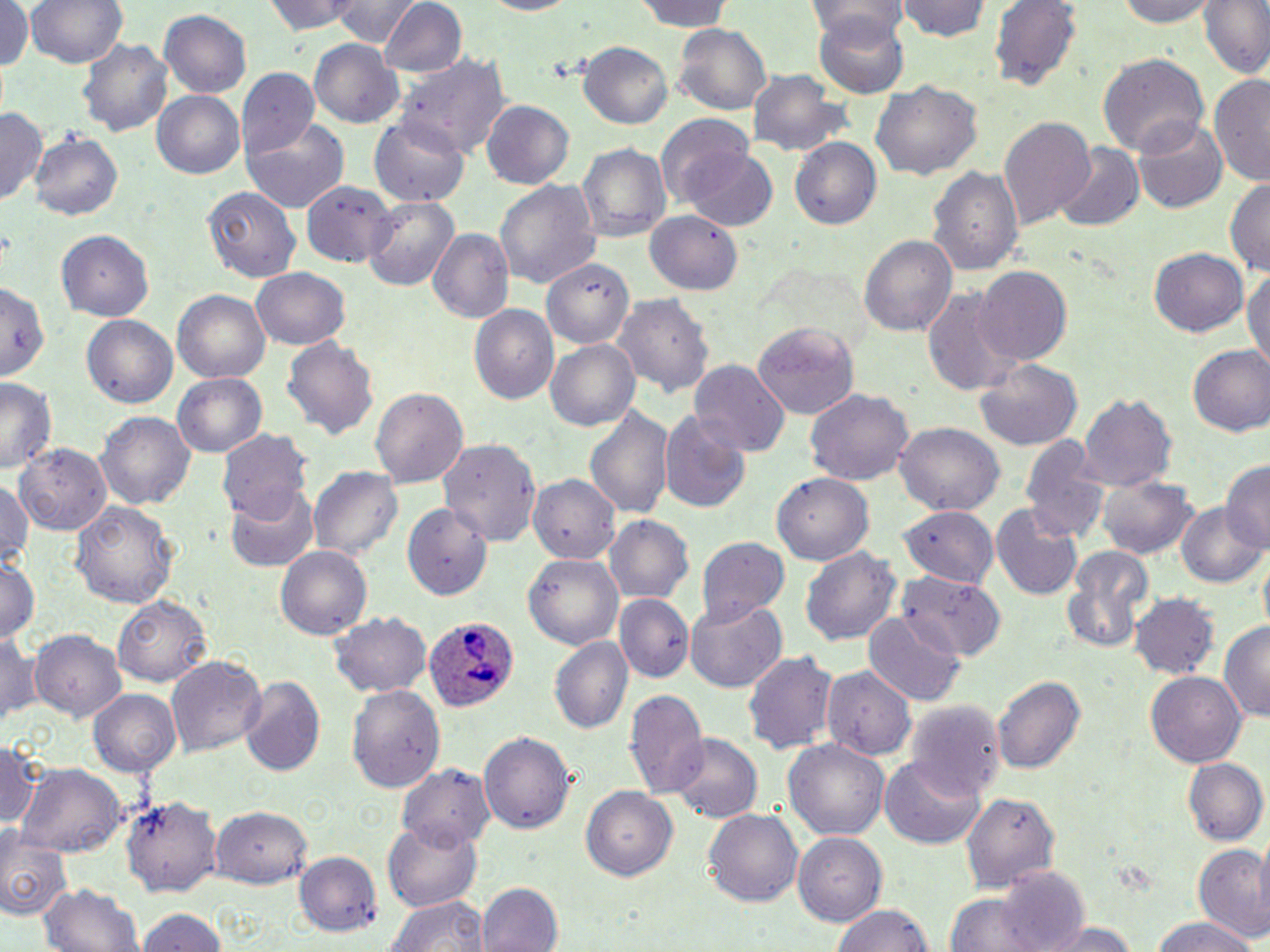
Summary:
  - Coordinate format: approximate bounding boxes as named x1/y1/x2/y2 corners in pixels
  - Uninfected red blood cell locations: (x1=28, y1=0, x2=127, y2=70), (x1=264, y1=0, x2=363, y2=35), (x1=330, y1=0, x2=416, y2=47), (x1=472, y1=0, x2=583, y2=17), (x1=626, y1=0, x2=736, y2=31), (x1=1111, y1=0, x2=1221, y2=26), (x1=1197, y1=0, x2=1270, y2=82), (x1=0, y1=1, x2=34, y2=79), (x1=899, y1=1, x2=994, y2=43), (x1=990, y1=1, x2=1082, y2=91), (x1=377, y1=2, x2=465, y2=78), (x1=803, y1=2, x2=909, y2=43), (x1=161, y1=9, x2=253, y2=98), (x1=814, y1=10, x2=910, y2=96), (x1=673, y1=24, x2=770, y2=113), (x1=80, y1=34, x2=176, y2=136), (x1=309, y1=39, x2=403, y2=127), (x1=578, y1=42, x2=674, y2=127), (x1=1098, y1=53, x2=1208, y2=160), (x1=399, y1=55, x2=508, y2=159), (x1=236, y1=68, x2=320, y2=156), (x1=746, y1=71, x2=853, y2=159), (x1=1210, y1=75, x2=1270, y2=186), (x1=871, y1=79, x2=983, y2=180), (x1=151, y1=91, x2=245, y2=180), (x1=482, y1=102, x2=573, y2=188), (x1=0, y1=108, x2=45, y2=207), (x1=369, y1=114, x2=471, y2=205), (x1=655, y1=115, x2=759, y2=213), (x1=997, y1=117, x2=1096, y2=228), (x1=1132, y1=119, x2=1228, y2=214), (x1=243, y1=120, x2=347, y2=213), (x1=29, y1=133, x2=122, y2=220), (x1=788, y1=137, x2=880, y2=230), (x1=578, y1=141, x2=670, y2=242), (x1=1052, y1=142, x2=1143, y2=234), (x1=682, y1=148, x2=778, y2=231), (x1=928, y1=165, x2=1023, y2=280), (x1=495, y1=177, x2=599, y2=293), (x1=302, y1=180, x2=400, y2=269), (x1=1225, y1=180, x2=1270, y2=277), (x1=203, y1=186, x2=299, y2=285), (x1=361, y1=196, x2=459, y2=293), (x1=646, y1=209, x2=744, y2=296), (x1=426, y1=228, x2=512, y2=326), (x1=55, y1=229, x2=154, y2=320), (x1=859, y1=233, x2=958, y2=337), (x1=1151, y1=247, x2=1249, y2=337), (x1=543, y1=261, x2=633, y2=350), (x1=1245, y1=266, x2=1270, y2=374), (x1=252, y1=267, x2=351, y2=349), (x1=977, y1=267, x2=1071, y2=365), (x1=0, y1=276, x2=48, y2=381), (x1=922, y1=287, x2=1023, y2=401), (x1=172, y1=288, x2=272, y2=384), (x1=615, y1=294, x2=713, y2=402), (x1=470, y1=303, x2=559, y2=405), (x1=83, y1=316, x2=177, y2=408), (x1=752, y1=323, x2=858, y2=419), (x1=283, y1=335, x2=380, y2=442), (x1=546, y1=339, x2=640, y2=433), (x1=1187, y1=346, x2=1270, y2=439), (x1=974, y1=356, x2=1083, y2=452), (x1=690, y1=361, x2=789, y2=460), (x1=171, y1=372, x2=268, y2=461), (x1=0, y1=379, x2=56, y2=473), (x1=370, y1=385, x2=468, y2=488), (x1=804, y1=388, x2=914, y2=487), (x1=1080, y1=395, x2=1177, y2=489), (x1=584, y1=406, x2=674, y2=519), (x1=659, y1=410, x2=752, y2=514), (x1=98, y1=414, x2=194, y2=509), (x1=891, y1=423, x2=1003, y2=516), (x1=219, y1=431, x2=313, y2=526), (x1=1018, y1=432, x2=1108, y2=554), (x1=437, y1=439, x2=539, y2=546), (x1=13, y1=443, x2=113, y2=536), (x1=1222, y1=461, x2=1270, y2=552), (x1=310, y1=467, x2=402, y2=564), (x1=772, y1=473, x2=874, y2=566), (x1=1097, y1=474, x2=1200, y2=563), (x1=531, y1=475, x2=621, y2=562), (x1=0, y1=481, x2=35, y2=571), (x1=227, y1=481, x2=319, y2=572), (x1=69, y1=499, x2=179, y2=608), (x1=1177, y1=502, x2=1269, y2=590), (x1=403, y1=503, x2=494, y2=601), (x1=991, y1=505, x2=1085, y2=603), (x1=898, y1=506, x2=997, y2=589), (x1=899, y1=507, x2=999, y2=590), (x1=605, y1=514, x2=692, y2=604), (x1=698, y1=537, x2=789, y2=624), (x1=1058, y1=544, x2=1154, y2=660), (x1=275, y1=545, x2=372, y2=640), (x1=802, y1=547, x2=898, y2=649), (x1=524, y1=553, x2=623, y2=649), (x1=0, y1=556, x2=39, y2=647), (x1=896, y1=574, x2=1006, y2=659), (x1=615, y1=594, x2=693, y2=682), (x1=1132, y1=594, x2=1218, y2=678), (x1=116, y1=597, x2=210, y2=688), (x1=685, y1=599, x2=787, y2=695), (x1=862, y1=609, x2=967, y2=708), (x1=328, y1=613, x2=431, y2=696), (x1=1219, y1=619, x2=1270, y2=722), (x1=0, y1=628, x2=39, y2=727), (x1=29, y1=631, x2=127, y2=720), (x1=550, y1=635, x2=633, y2=734), (x1=741, y1=648, x2=842, y2=753), (x1=167, y1=655, x2=267, y2=760), (x1=820, y1=665, x2=912, y2=759), (x1=1145, y1=670, x2=1246, y2=768), (x1=994, y1=674, x2=1085, y2=778), (x1=236, y1=676, x2=325, y2=779), (x1=348, y1=685, x2=446, y2=793), (x1=625, y1=687, x2=708, y2=799), (x1=89, y1=689, x2=180, y2=777), (x1=906, y1=701, x2=1004, y2=801), (x1=480, y1=731, x2=578, y2=834), (x1=669, y1=736, x2=762, y2=822), (x1=785, y1=739, x2=888, y2=844), (x1=0, y1=741, x2=43, y2=831), (x1=883, y1=756, x2=984, y2=849), (x1=1185, y1=758, x2=1267, y2=845), (x1=16, y1=764, x2=125, y2=857), (x1=398, y1=764, x2=492, y2=849), (x1=580, y1=786, x2=677, y2=882), (x1=961, y1=795, x2=1058, y2=895), (x1=124, y1=796, x2=219, y2=897), (x1=210, y1=805, x2=312, y2=889), (x1=703, y1=808, x2=803, y2=907), (x1=386, y1=820, x2=482, y2=909), (x1=0, y1=827, x2=72, y2=922), (x1=795, y1=833, x2=891, y2=924), (x1=1191, y1=844, x2=1270, y2=943), (x1=296, y1=851, x2=381, y2=937), (x1=993, y1=867, x2=1093, y2=952), (x1=37, y1=882, x2=145, y2=952), (x1=478, y1=884, x2=561, y2=952), (x1=383, y1=892, x2=486, y2=952), (x1=943, y1=895, x2=1051, y2=952), (x1=828, y1=904, x2=936, y2=952), (x1=135, y1=907, x2=228, y2=952), (x1=1149, y1=916, x2=1255, y2=952), (x1=1039, y1=920, x2=1139, y2=952)
  - Plasmodium ovale-infected red blood cell locations: (x1=424, y1=617, x2=515, y2=715)
  - Slide-level diagnosis: Plasmodium ovale
  - Preparation: thin blood smear
  - Image size: 1270×952 pixels
  - Stain: May-Grünwald-Giemsa
  - Field of view: one of a larger specimen
  - Magnification: 1000x
  - Modality: optical microscopy